Identify the parasite.
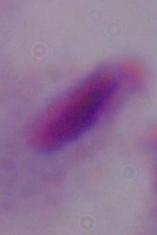
A trichomonad.

magnification: 1000x
modality: photomicrograph